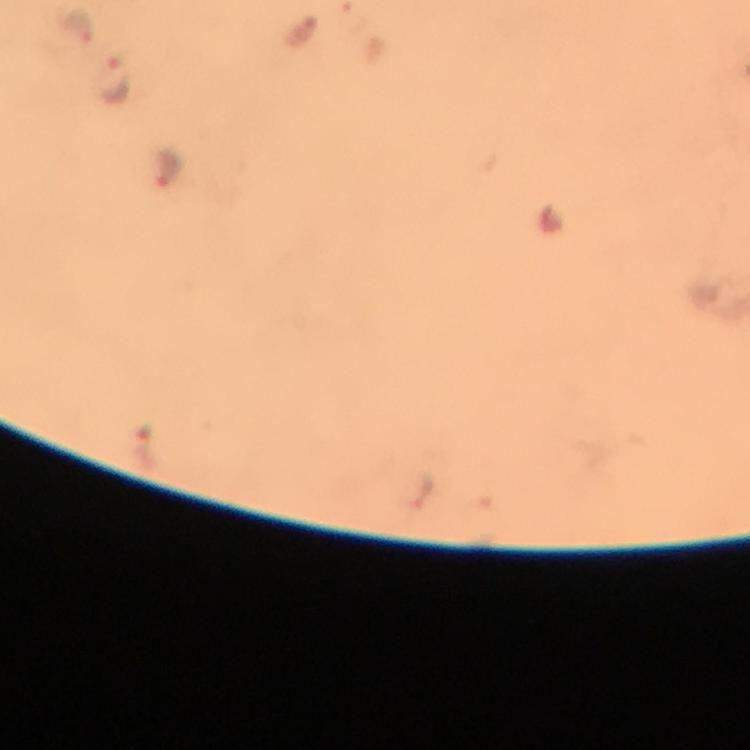

Approximate centers as {x, y} in pixels.
Summary:
  - Plasmodium parasite locations: {77, 26}, {117, 82}, {170, 169}
  - Preparation: thick blood smear
  - Cropped from: one field of view
  - Capture: smartphone photograph through a microscope
  - Context: from a malaria diagnostic workup
  - Image size: 750×750 pixels
  - Immersion oil: applied
  - Stain: Giemsa
  - Magnification: 100x